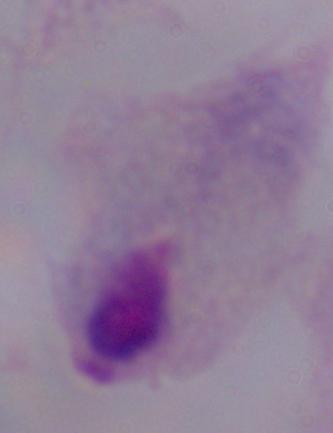

Photomicrograph. Captured at 1000x magnification. A trichomonad is seen.